Locate and identify every blood parasite.
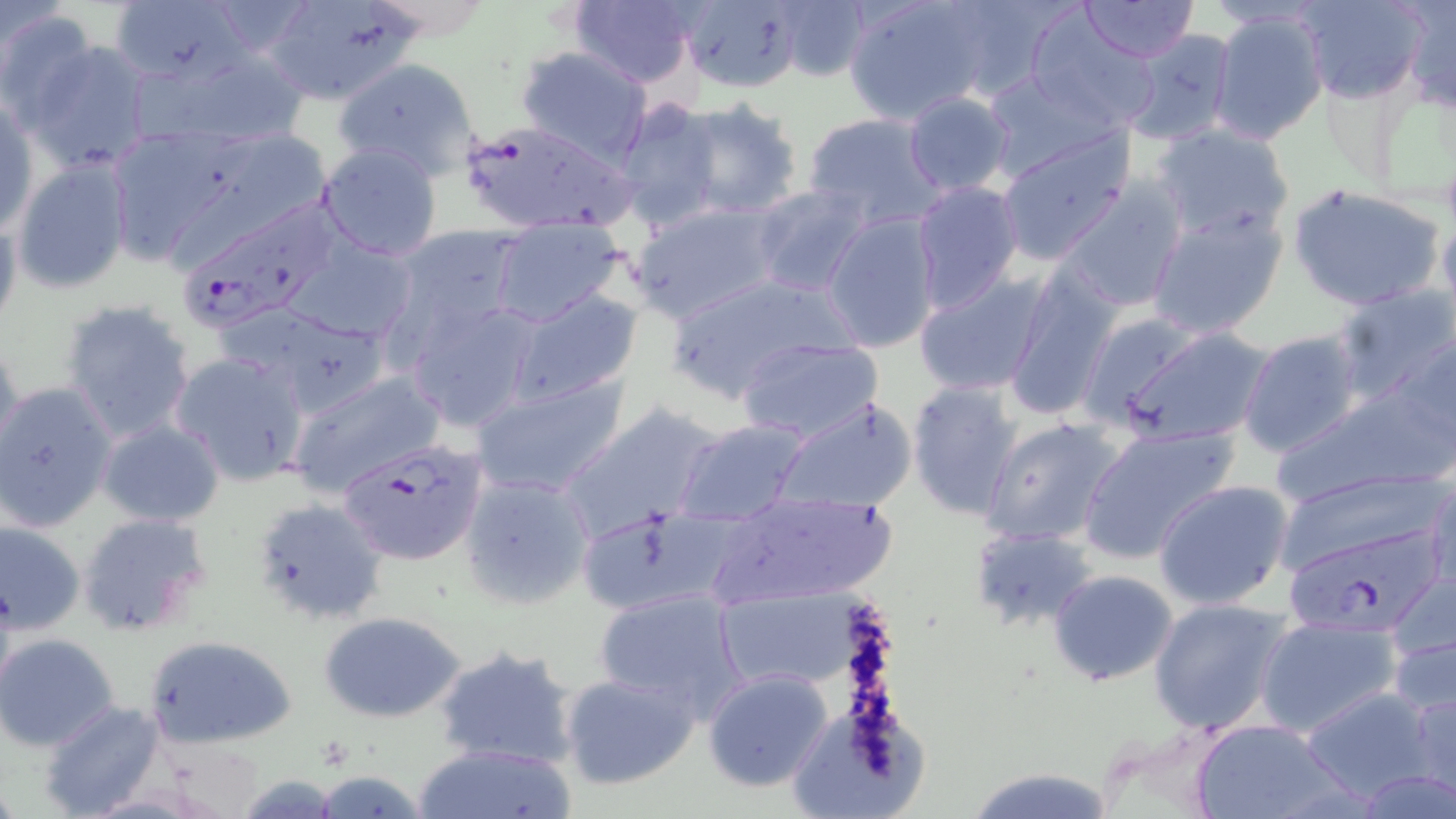

Approximate bounding boxes as [x1, y1, x2, y2] in pixels.
Plasmodium falciparum-infected red blood cells: [460, 121, 630, 234], [185, 186, 340, 330], [339, 438, 489, 567], [1283, 527, 1449, 629].
No Plasmodium ovale, Plasmodium malariae, Plasmodium vivax, Babesia divergens, or Trypanosoma brucei observed.

Uninfected red blood cell locations: [260, 0, 425, 104], [675, 0, 807, 92], [843, 0, 998, 124], [1079, 0, 1198, 64], [1298, 0, 1428, 104], [1399, 0, 1456, 110], [109, 1, 245, 86], [568, 1, 699, 87], [769, 1, 871, 84], [0, 8, 99, 125], [1207, 8, 1329, 146], [1024, 13, 1158, 130], [1120, 30, 1240, 147], [20, 38, 156, 172], [146, 43, 314, 151], [516, 45, 653, 164], [335, 57, 479, 184], [980, 71, 1120, 182], [904, 91, 1014, 196], [1, 95, 38, 236], [675, 98, 806, 218], [616, 100, 722, 229], [804, 111, 946, 231], [1150, 123, 1295, 242], [104, 124, 238, 264], [994, 130, 1135, 265], [172, 135, 327, 275], [317, 142, 444, 262], [10, 159, 133, 292], [1055, 177, 1189, 313], [912, 181, 1024, 313], [1288, 183, 1447, 312], [750, 184, 874, 298], [629, 201, 786, 323], [1145, 203, 1289, 339], [821, 211, 942, 352], [0, 212, 22, 341], [489, 218, 628, 328], [388, 225, 526, 342], [286, 238, 420, 346], [1000, 264, 1122, 423], [913, 270, 1049, 397], [666, 272, 853, 400], [1330, 284, 1455, 404], [508, 289, 643, 402], [403, 297, 542, 432], [60, 300, 197, 443], [235, 307, 390, 414], [1105, 326, 1273, 446], [1239, 330, 1364, 459], [1392, 331, 1455, 462], [735, 335, 885, 441], [0, 339, 25, 464], [169, 350, 311, 487], [287, 368, 444, 496], [470, 372, 630, 498], [906, 380, 1024, 519], [1, 381, 118, 533], [1269, 384, 1452, 505], [774, 396, 919, 513], [558, 403, 724, 539], [979, 415, 1125, 546], [674, 418, 811, 526], [98, 419, 224, 527], [1077, 424, 1239, 565], [459, 469, 596, 608], [1275, 469, 1446, 578], [1424, 469, 1455, 601], [1154, 480, 1295, 610], [702, 489, 900, 610], [251, 498, 390, 627], [77, 512, 212, 636], [0, 520, 86, 634], [968, 526, 1097, 632], [1047, 568, 1179, 687], [1382, 569, 1456, 696], [714, 587, 865, 693], [594, 588, 748, 716], [1148, 597, 1292, 735], [317, 610, 468, 723], [1256, 613, 1401, 738], [143, 633, 298, 749], [0, 634, 120, 749], [432, 645, 582, 771], [560, 669, 701, 791], [703, 669, 835, 793], [1403, 680, 1456, 799], [1295, 685, 1442, 803], [39, 700, 165, 818], [790, 702, 944, 814], [1189, 717, 1347, 819], [412, 742, 578, 819], [961, 765, 1121, 819], [1353, 767, 1456, 819], [312, 771, 429, 817]. Slide-level diagnosis: Plasmodium falciparum. 1000x magnification. One field of a larger specimen. Optical microscopy. Thin blood film. May-Grünwald-Giemsa stain. Image is 1456×819 pixels.